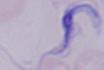 A trypanosome is shown. 1000x magnification. Micrograph.